Give the extent of all uninfected red blood cells.
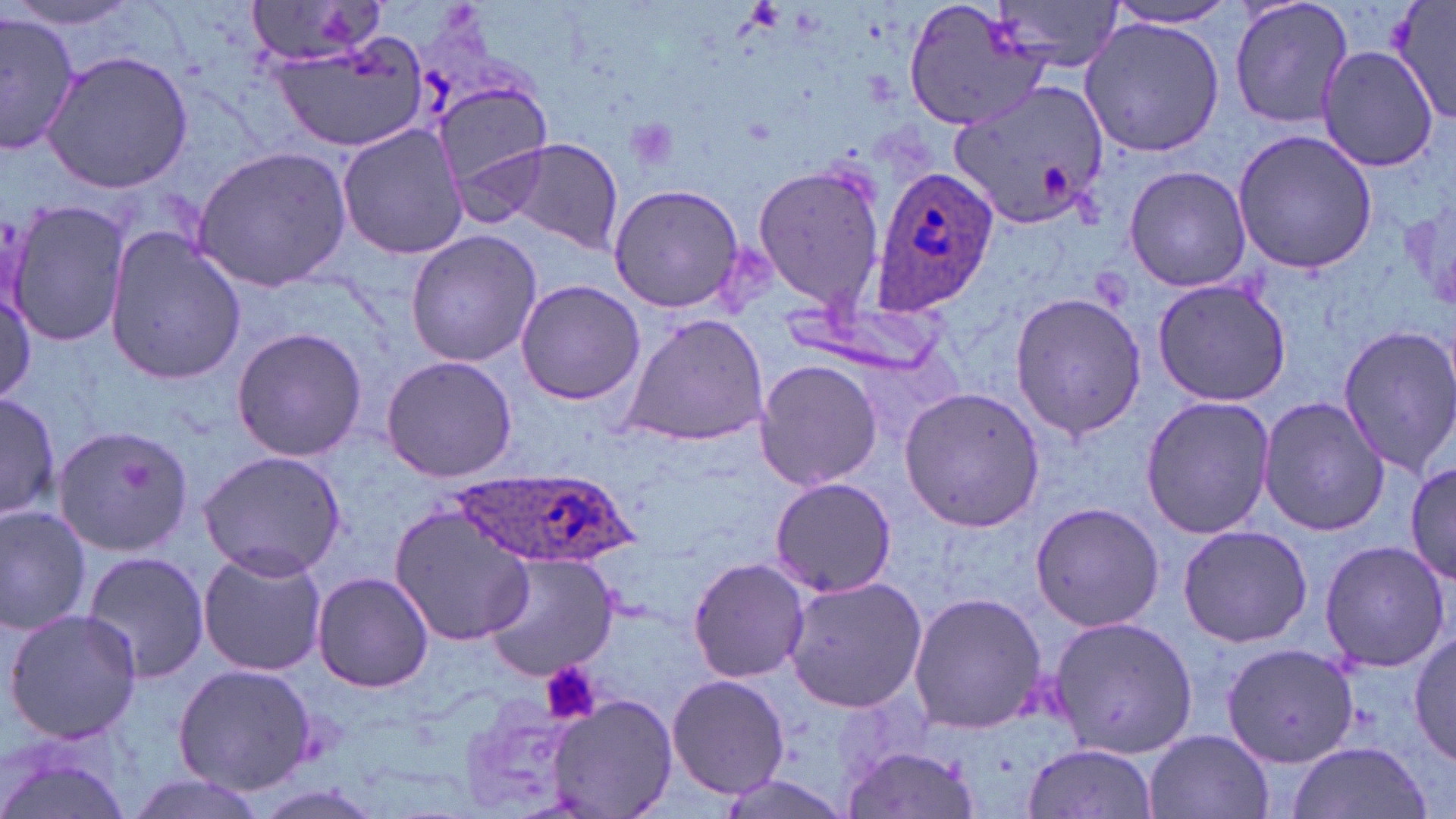

Approximate bounding boxes as (x1, y1, x2, y2) in pixels.
Uninfected red blood cells: (241, 0, 392, 69), (904, 0, 1054, 131), (990, 0, 1124, 74), (1230, 0, 1354, 129), (1385, 0, 1456, 123), (1102, 3, 1245, 31), (0, 10, 80, 157), (1079, 17, 1224, 158), (271, 32, 425, 155), (1316, 46, 1438, 171), (41, 49, 195, 194), (435, 81, 553, 203), (947, 81, 1108, 227), (337, 124, 472, 260), (1232, 128, 1379, 275), (506, 139, 624, 253), (192, 146, 352, 290), (750, 160, 886, 311), (1123, 165, 1251, 292), (607, 182, 746, 314), (7, 198, 129, 346), (103, 228, 245, 387), (405, 230, 542, 368), (514, 279, 644, 407), (1152, 279, 1291, 407), (0, 280, 36, 409), (1009, 291, 1149, 441), (617, 313, 771, 449), (1334, 325, 1456, 476), (230, 326, 368, 463), (379, 355, 518, 483), (753, 357, 882, 492), (901, 387, 1046, 532), (0, 389, 62, 524), (1140, 394, 1276, 541), (1256, 396, 1391, 536), (49, 423, 193, 557), (197, 450, 348, 578), (1405, 461, 1456, 586), (768, 476, 897, 598), (0, 502, 95, 638), (1029, 502, 1166, 632), (389, 504, 536, 646), (1176, 524, 1313, 647), (1318, 538, 1451, 674), (196, 546, 329, 677), (81, 549, 210, 683), (482, 553, 621, 678), (686, 557, 811, 683), (311, 570, 435, 692), (781, 573, 927, 714), (907, 592, 1046, 734), (3, 606, 144, 745), (1044, 616, 1200, 756), (1409, 630, 1456, 767), (1221, 642, 1358, 770), (171, 663, 319, 794), (664, 674, 791, 800), (458, 692, 588, 816), (546, 694, 676, 819), (1143, 728, 1274, 819), (0, 736, 136, 819), (1284, 739, 1436, 819), (1022, 742, 1159, 819), (841, 746, 983, 819), (118, 774, 274, 819).

Plasmodium ovale-infected red blood cell locations: (870, 166, 999, 315), (444, 468, 642, 567). Platelet locations: (625, 118, 679, 175), (539, 662, 600, 724). Slide-level diagnosis: Plasmodium ovale. Image is 1456×819 pixels. One field of a larger specimen. Optical microscopy. May-Grünwald-Giemsa-stained preparation. Captured at 1000x magnification. Thin blood film.